Locate and identify every blood parasite.
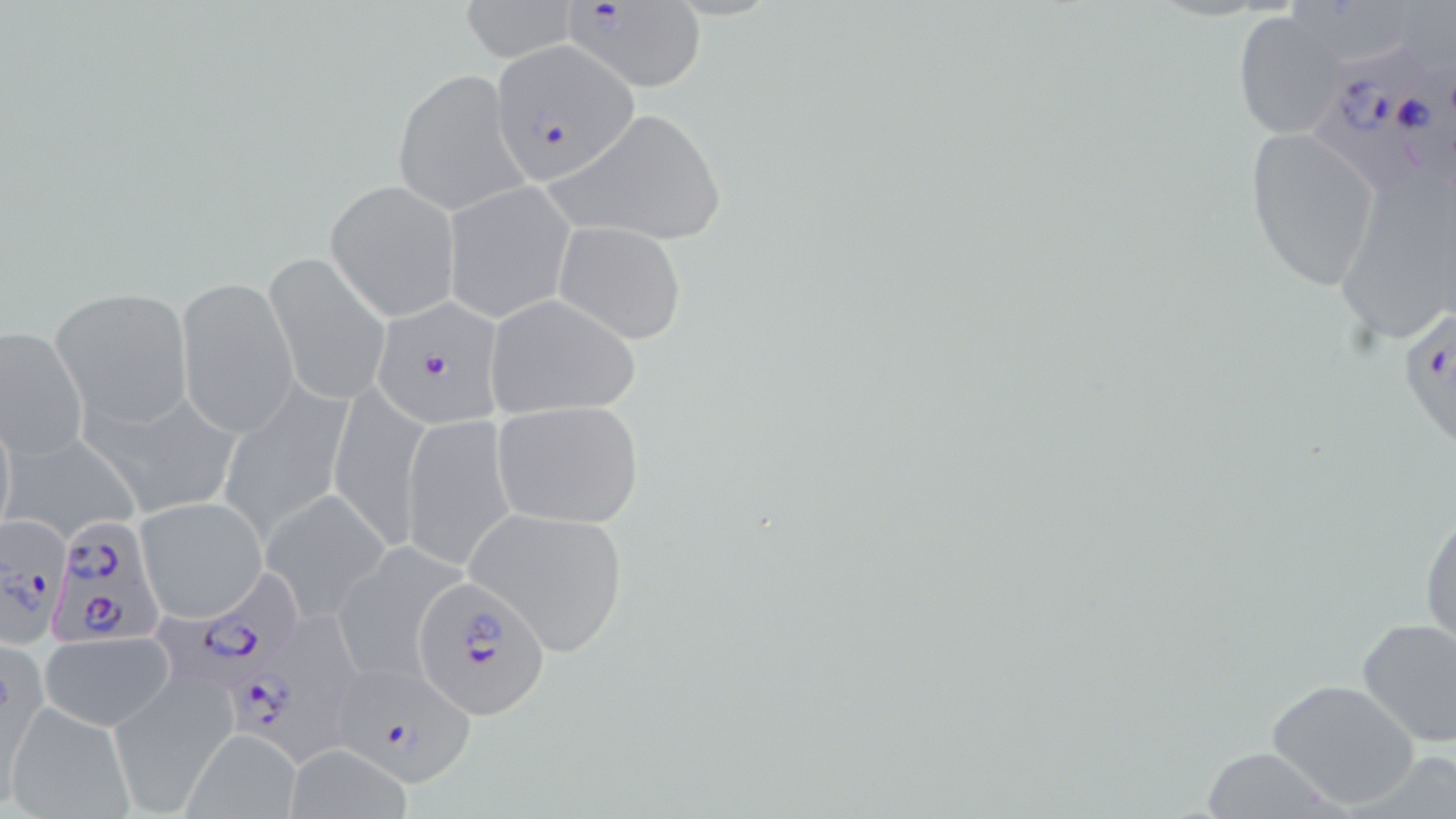
Approximate bounding boxes as (x1, y1, x2, y2) in pixels.
Plasmodium falciparum-infected red blood cells: (559, 0, 709, 94), (491, 43, 637, 185), (1314, 43, 1456, 196), (371, 296, 509, 430), (1396, 307, 1456, 450), (1, 511, 71, 642), (44, 515, 170, 649), (166, 566, 314, 688), (414, 578, 552, 719), (231, 614, 386, 775), (334, 665, 479, 785).
No Plasmodium ovale, Plasmodium malariae, Plasmodium vivax, Babesia divergens, or Trypanosoma brucei observed.

Uninfected red blood cell locations: (458, 0, 581, 63), (1282, 0, 1410, 70), (1233, 10, 1348, 140), (391, 69, 528, 214), (551, 108, 729, 247), (1245, 127, 1382, 293), (1334, 166, 1455, 347), (325, 179, 461, 322), (442, 179, 577, 323), (552, 221, 688, 345), (264, 252, 393, 407), (176, 278, 299, 437), (51, 288, 192, 429), (484, 295, 641, 417), (0, 322, 88, 464), (329, 379, 432, 546), (217, 382, 356, 543), (83, 385, 246, 521), (492, 401, 645, 528), (400, 415, 519, 571), (5, 430, 144, 544), (262, 490, 390, 620), (136, 496, 268, 623), (1420, 499, 1455, 654), (464, 505, 629, 656), (331, 540, 470, 683), (1354, 617, 1456, 748), (40, 632, 174, 726), (1, 643, 48, 798), (108, 677, 234, 813), (1265, 678, 1421, 811), (4, 703, 135, 819), (182, 729, 303, 819), (283, 744, 414, 819). Slide-level diagnosis: Plasmodium falciparum. Single field of view. Light microscopy. May-Grünwald-Giemsa-stained preparation. Thin blood smear. 1000x magnification. Image is 1456×819 pixels.